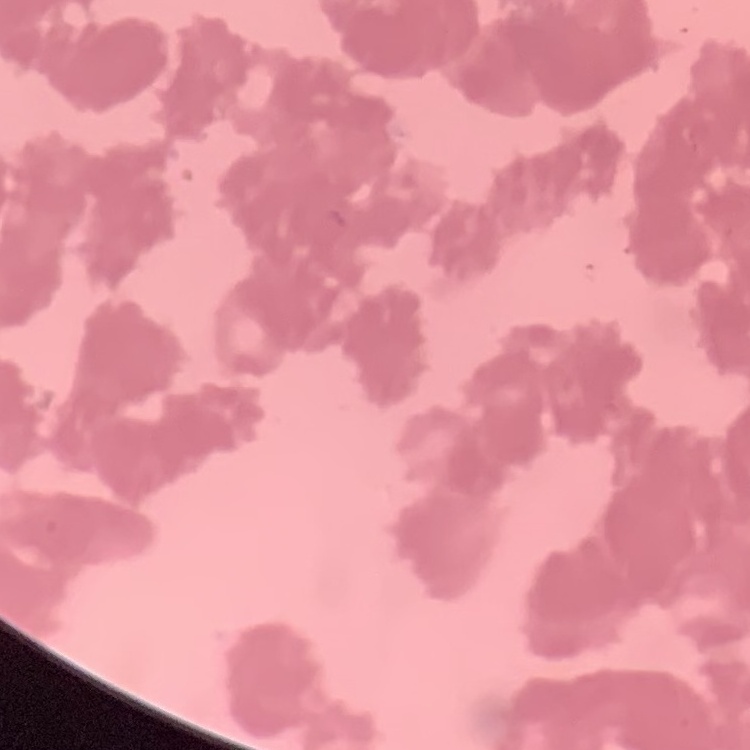 The red blood cells show rouleaux formation. Stained with either Field's or Giemsa. Square crop of a larger photomicrograph. Thin peripheral smear.